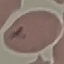

result = malaria parasites identified
preparation = thin smear
capture = smartphone through the microscope eyepiece
image type = cell patch, automatically extracted from a larger field of view and resized to 64 × 64 pixels
stain = Giemsa